Report the malaria status of this cell.
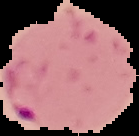
It is parasitized.

image type = segmented cell region with the area outside set to black
image size = 139×136 pixels
preparation = thin blood film